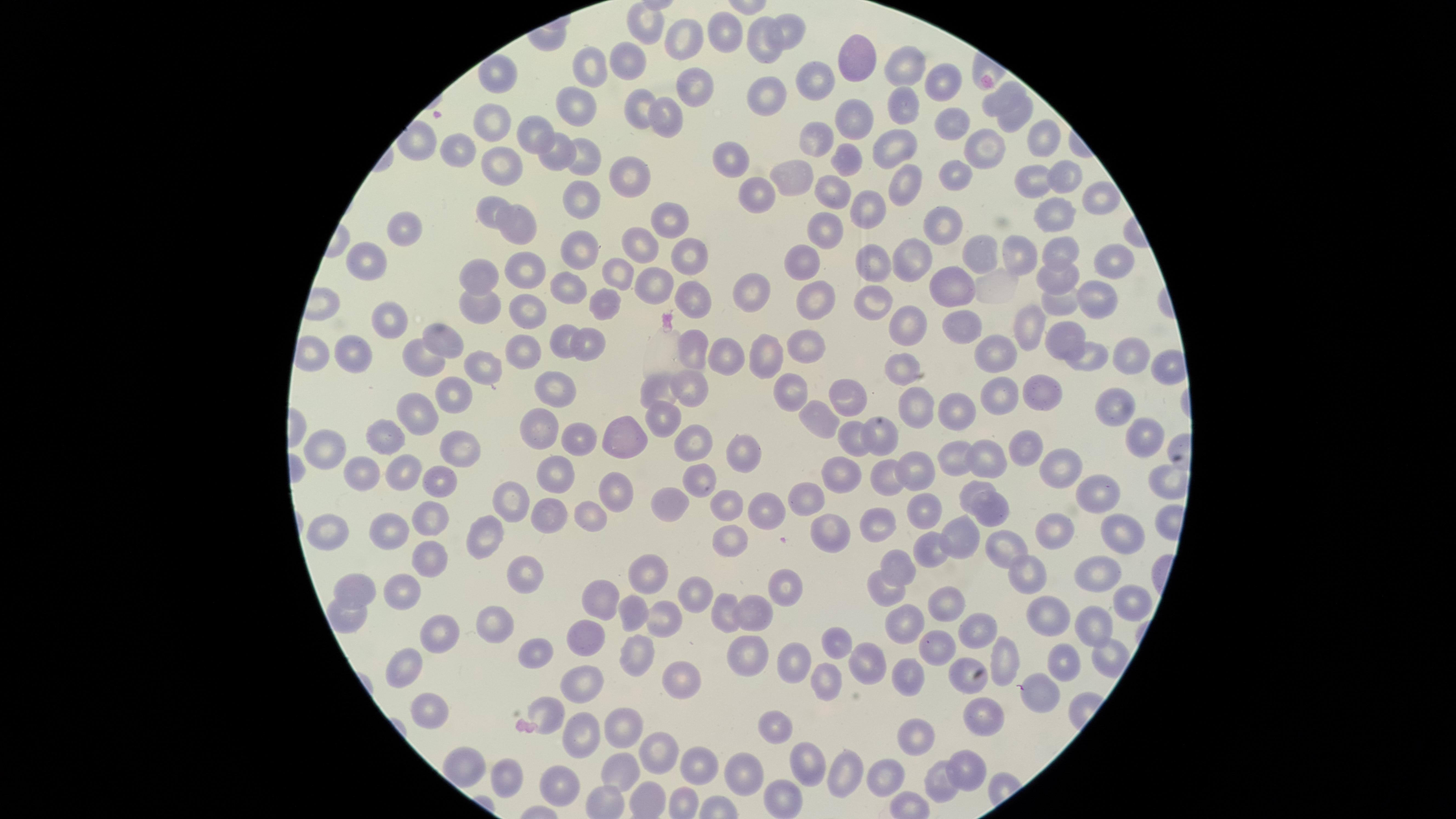 Approximate marker points, in pixels from the top-left corner. Uninfected RBCs: (x=648, y=20), (x=795, y=27), (x=727, y=35), (x=690, y=38), (x=759, y=44), (x=632, y=58), (x=860, y=60), (x=905, y=67), (x=500, y=71), (x=596, y=71), (x=824, y=74), (x=946, y=80), (x=692, y=85), (x=764, y=91), (x=1002, y=94), (x=635, y=104), (x=910, y=108), (x=578, y=111), (x=667, y=116), (x=1020, y=116), (x=856, y=119), (x=954, y=125), (x=535, y=129), (x=497, y=130), (x=818, y=136), (x=1043, y=139), (x=987, y=141), (x=895, y=147), (x=455, y=148), (x=555, y=154), (x=584, y=156), (x=732, y=160), (x=849, y=163), (x=502, y=165), (x=963, y=171), (x=628, y=172), (x=1067, y=174), (x=790, y=177), (x=1035, y=180), (x=905, y=185), (x=838, y=193), (x=1097, y=196), (x=583, y=197), (x=757, y=199), (x=484, y=208), (x=870, y=208), (x=667, y=217), (x=1053, y=217), (x=402, y=227), (x=826, y=227), (x=945, y=228), (x=520, y=229), (x=638, y=246), (x=1058, y=248), (x=579, y=249), (x=683, y=250), (x=1022, y=252), (x=986, y=254), (x=913, y=258), (x=366, y=260), (x=799, y=260), (x=876, y=263), (x=1107, y=267), (x=529, y=272), (x=619, y=272), (x=485, y=274), (x=1053, y=276), (x=951, y=283), (x=654, y=285), (x=571, y=287), (x=756, y=290), (x=815, y=295), (x=870, y=295), (x=1095, y=297), (x=610, y=300), (x=692, y=300), (x=486, y=308), (x=1061, y=308), (x=529, y=311), (x=905, y=317), (x=388, y=320), (x=1028, y=328), (x=961, y=330), (x=1065, y=334), (x=562, y=337), (x=444, y=339), (x=804, y=343), (x=521, y=347), (x=353, y=348), (x=586, y=348), (x=692, y=350), (x=728, y=353), (x=774, y=353), (x=995, y=353), (x=1123, y=354), (x=429, y=358), (x=1084, y=358), (x=491, y=364), (x=902, y=374), (x=552, y=380), (x=690, y=386), (x=1049, y=387), (x=842, y=389), (x=657, y=390), (x=998, y=393), (x=452, y=394), (x=787, y=397), (x=422, y=408), (x=925, y=408), (x=954, y=408), (x=1117, y=408), (x=815, y=416), (x=660, y=420), (x=538, y=423), (x=617, y=433), (x=394, y=434), (x=882, y=435), (x=851, y=436), (x=579, y=438), (x=336, y=444), (x=452, y=444), (x=1025, y=444), (x=1135, y=444), (x=694, y=445), (x=989, y=455), (x=958, y=456), (x=1062, y=456), (x=741, y=457), (x=367, y=469), (x=911, y=470), (x=409, y=472), (x=548, y=475), (x=702, y=477), (x=844, y=478), (x=883, y=479), (x=445, y=480), (x=1095, y=486), (x=970, y=487), (x=618, y=494), (x=811, y=497), (x=507, y=498), (x=673, y=500), (x=916, y=506), (x=722, y=507), (x=768, y=511), (x=990, y=516), (x=546, y=518), (x=584, y=518), (x=428, y=521), (x=875, y=524), (x=395, y=525), (x=328, y=529), (x=835, y=530), (x=1057, y=532), (x=1128, y=534), (x=484, y=536), (x=962, y=538), (x=727, y=544), (x=1003, y=545), (x=934, y=553), (x=433, y=562), (x=903, y=563), (x=522, y=573), (x=649, y=575), (x=1098, y=576), (x=1030, y=578), (x=784, y=579), (x=887, y=586), (x=356, y=587), (x=406, y=588), (x=695, y=590), (x=602, y=593), (x=950, y=600), (x=1125, y=603), (x=757, y=605), (x=636, y=609), (x=725, y=609), (x=1053, y=611), (x=659, y=616), (x=908, y=618), (x=1092, y=623), (x=499, y=624), (x=979, y=624), (x=439, y=635), (x=586, y=636), (x=830, y=639), (x=939, y=645), (x=533, y=650), (x=739, y=653), (x=635, y=657), (x=1002, y=658), (x=789, y=659), (x=862, y=661), (x=408, y=664), (x=960, y=664), (x=1065, y=665), (x=678, y=673), (x=825, y=678), (x=913, y=679), (x=591, y=684), (x=1044, y=695), (x=429, y=702), (x=545, y=710), (x=988, y=718), (x=622, y=720), (x=582, y=729), (x=776, y=730), (x=922, y=738), (x=664, y=750), (x=810, y=755), (x=967, y=760), (x=698, y=762), (x=847, y=768), (x=626, y=769), (x=514, y=772), (x=744, y=772), (x=887, y=773), (x=561, y=787), (x=940, y=789), (x=779, y=793). One field of view of the specimen. Photographed with a smartphone camera through the microscope eyepiece. Presence: no malaria parasites detected. Image is 1456×819 pixels. Thin smear of blood. The visible region is circular. Giemsa-stained preparation.